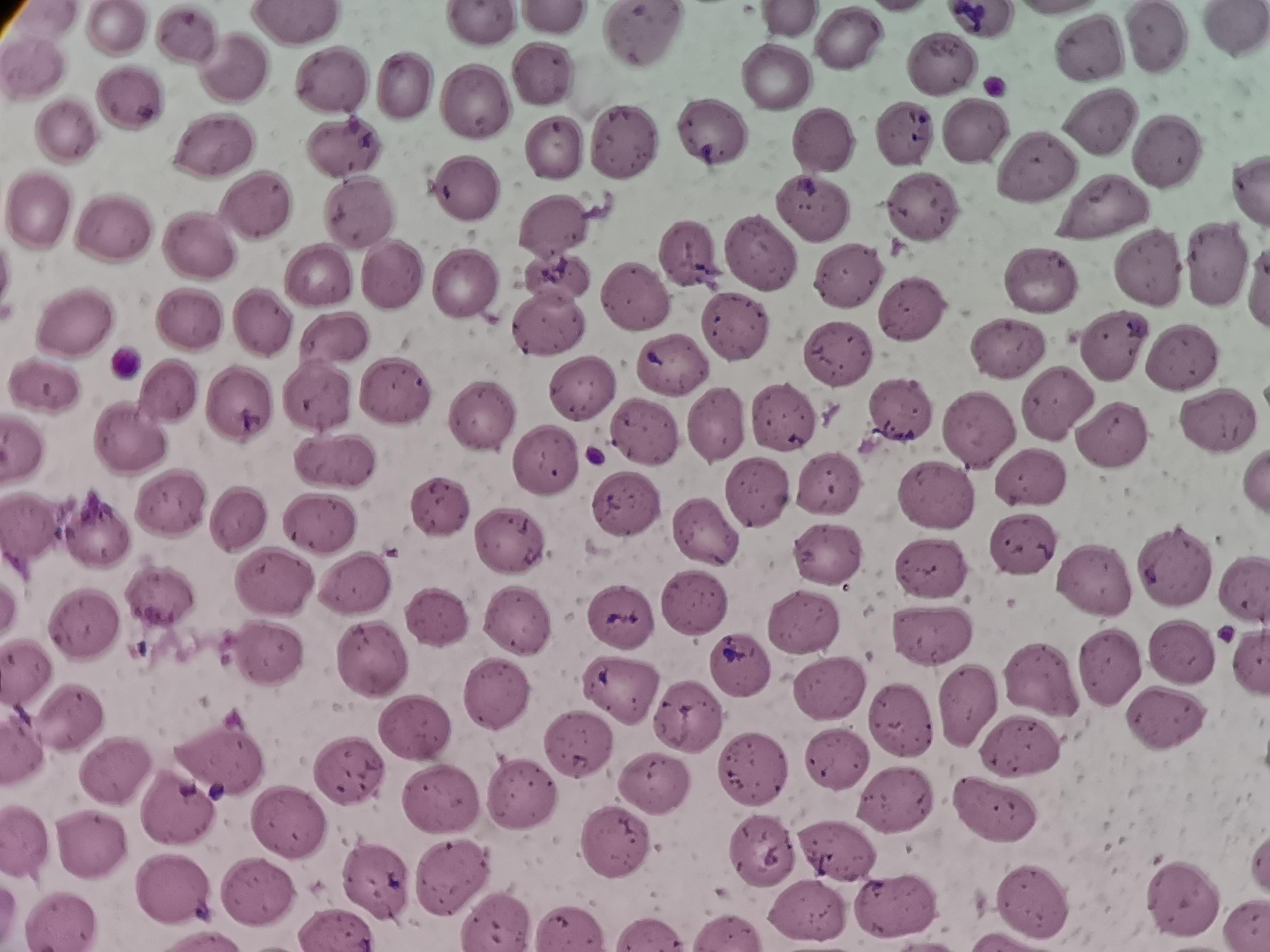
{
  "cell_locations": "approximate centers as {x, y} in pixels: {302, 22}, {118, 24}, {484, 28}, {190, 30}, {1233, 33}, {645, 35}, {1154, 39}, {853, 40}, {1096, 48}, {937, 61}, {229, 64}, {534, 75}, {774, 76}, {329, 78}, {403, 88}, {135, 92}, {471, 102}, {1100, 118}, {971, 125}, {70, 130}, {715, 130}, {904, 135}, {822, 142}, {217, 143}, {616, 143}, {548, 146}, {344, 147}, {1166, 153}, {1041, 162}, {466, 192}, {1108, 197}, {259, 202}, {42, 204}, {809, 206}, {920, 207}, {360, 209}, {113, 219}, {558, 229}, {677, 251}, {204, 252}, {765, 252}, {1141, 259}, {1222, 263}, {846, 271}, {391, 273}, {319, 274}, {1055, 279}, {557, 280}, {461, 281}, {631, 296}, {912, 311}, {185, 316}, {545, 317}, {84, 323}, {268, 323}, {734, 325}, {336, 337}, {1119, 341}, {1002, 348}, {838, 351}, {1185, 367}, {675, 370}, {48, 386}, {175, 390}, {392, 390}, {579, 396}, {318, 397}, {243, 403}, {1064, 404}, {478, 413}, {785, 416}, {1216, 417}, {722, 423}, {979, 429}, {1114, 434}, {134, 435}, {652, 435}, {538, 465}, {335, 466}, {835, 490}, {762, 494}, {931, 494}, {625, 495}, {177, 506}, {445, 511}, {242, 515}, {34, 525}, {103, 526}, {318, 526}, {703, 538}, {1020, 538}, {508, 544}, {833, 549}, {1173, 565}, {932, 566}, {1090, 578}, {274, 580}, {1245, 586}, {361, 588}, {162, 599}, {684, 603}, {436, 617}, {618, 618}, {516, 620}, {810, 620}, {86, 628}, {934, 639}, {1182, 652}, {266, 653}, {737, 657}, {375, 658}, {1112, 664}, {1055, 676}, {28, 677}, {495, 684}, {831, 686}, {619, 692}, {974, 706}, {77, 717}, {1172, 719}, {695, 722}, {413, 726}, {1021, 742}, {574, 746}, {837, 758}, {221, 760}, {117, 766}, {342, 769}, {747, 772}, {652, 786}, {516, 787}, {901, 800}, {437, 802}, {179, 803}, {997, 803}, {287, 819}, {86, 835}, {613, 842}, {757, 846}, {836, 851}, {453, 870}, {172, 887}, {255, 887}, {367, 887}, {1185, 895}, {1035, 901}, {818, 906}, {895, 909}, {502, 922}",
  "capture": "smartphone camera at the microscope eyepiece",
  "stain": "Giemsa",
  "preparation": "thin smear",
  "image_size": "1270×952 pixels",
  "field_of_view": "single"
}